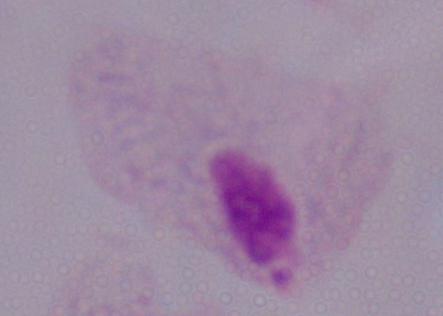
A trichomonad is seen. Captured at 1000x magnification. Micrograph.